Report the malaria status of this cell.
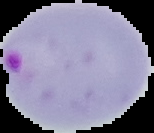

Parasitized.

From a thin blood smear. Segmented cell region on a black background. Image is 154×133 pixels.